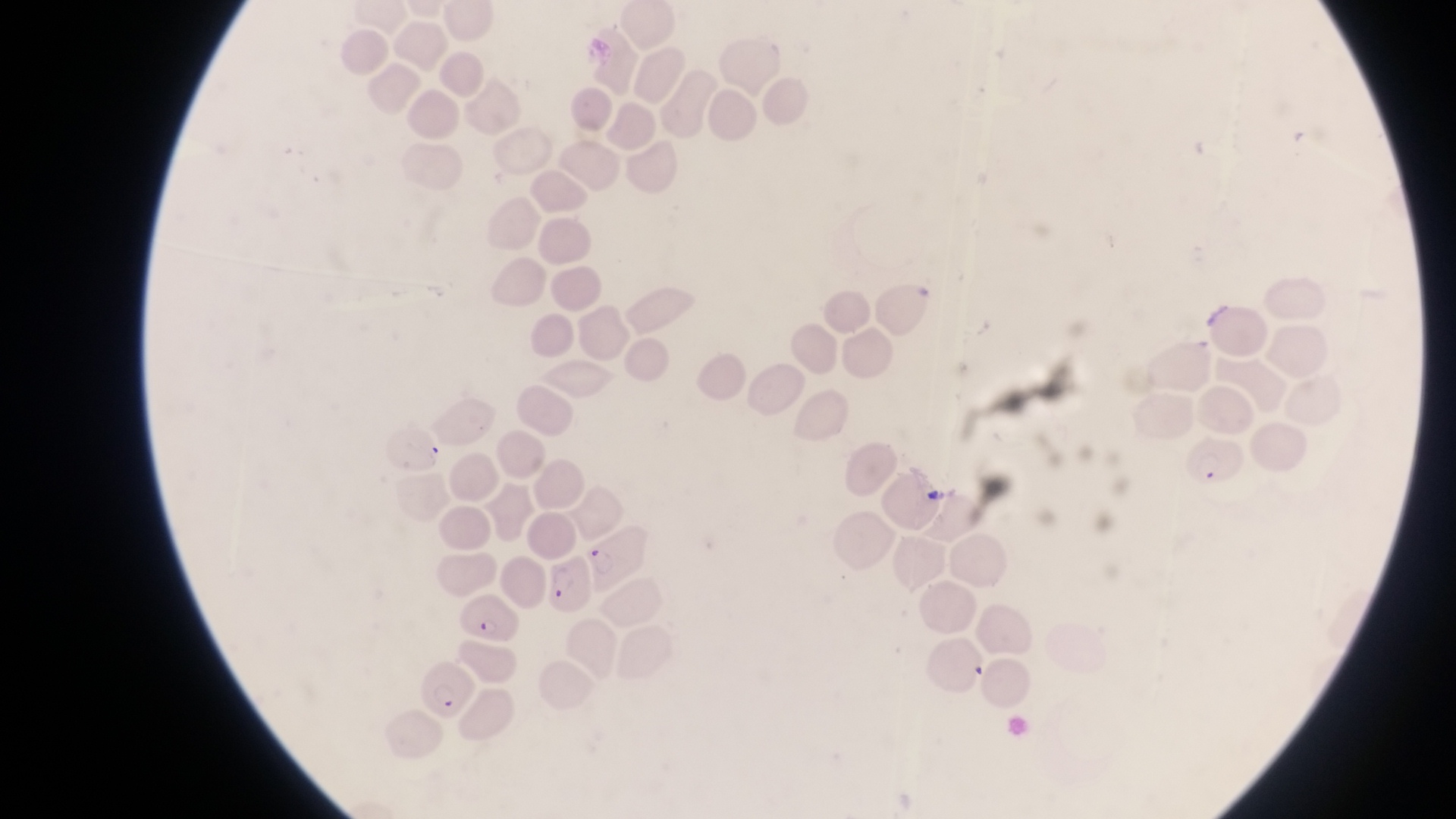
Approximate bounding boxes as (left, top, right, bottom) in pixels.
Summary:
  - Artifact (platelet-like body, stain precipitate, or debris) locations: (925, 481, 949, 511)
  - Parasitised red blood cell locations: (1192, 428, 1248, 491), (589, 529, 648, 587), (547, 560, 590, 616), (462, 595, 521, 645), (420, 660, 479, 721)
  - Capture: smartphone photograph through the eyepiece of an Olympus CX-23 microscope
  - Country: Uganda
  - Magnification: 1000x
  - Preparation: thin blood film
  - Image size: 1456×819 pixels
  - Field of view: single